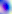
modality: photomicrograph
magnification: 400x
identification: Toxoplasma gondii